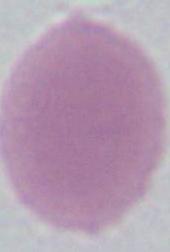
{
  "magnification": "1000x",
  "identification": "red blood cell",
  "modality": "photomicrograph"
}